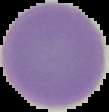
result = negative for Plasmodium parasites
image size = 109×112 pixels
preparation = thin blood smear
image type = segmented cell region with the area outside set to black